Assess the morphology of the red blood cells.
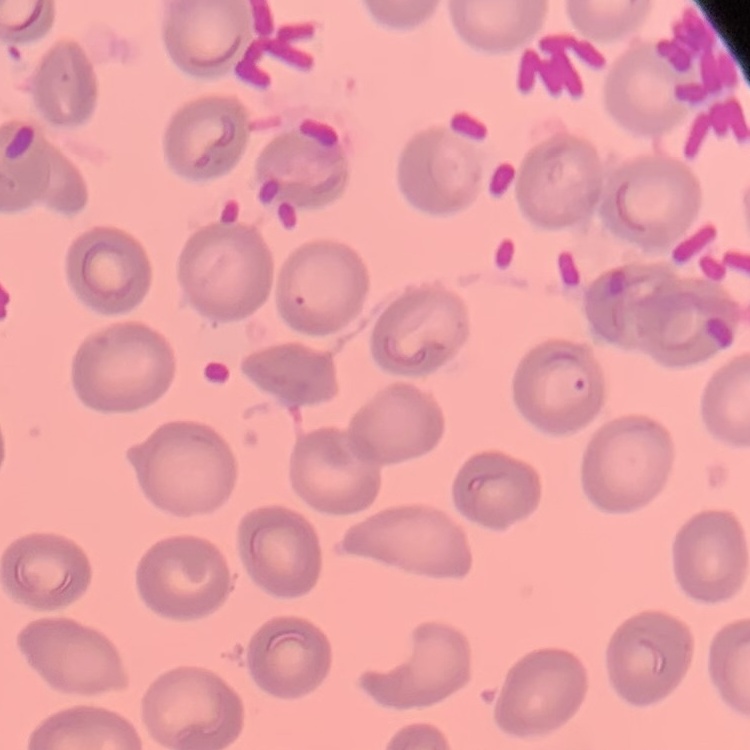

They show no rouleaux formation.

Summary:
  - Preparation: thin peripheral smear
  - Image type: square crop of a larger photomicrograph
  - Stain: Field's or Giemsa